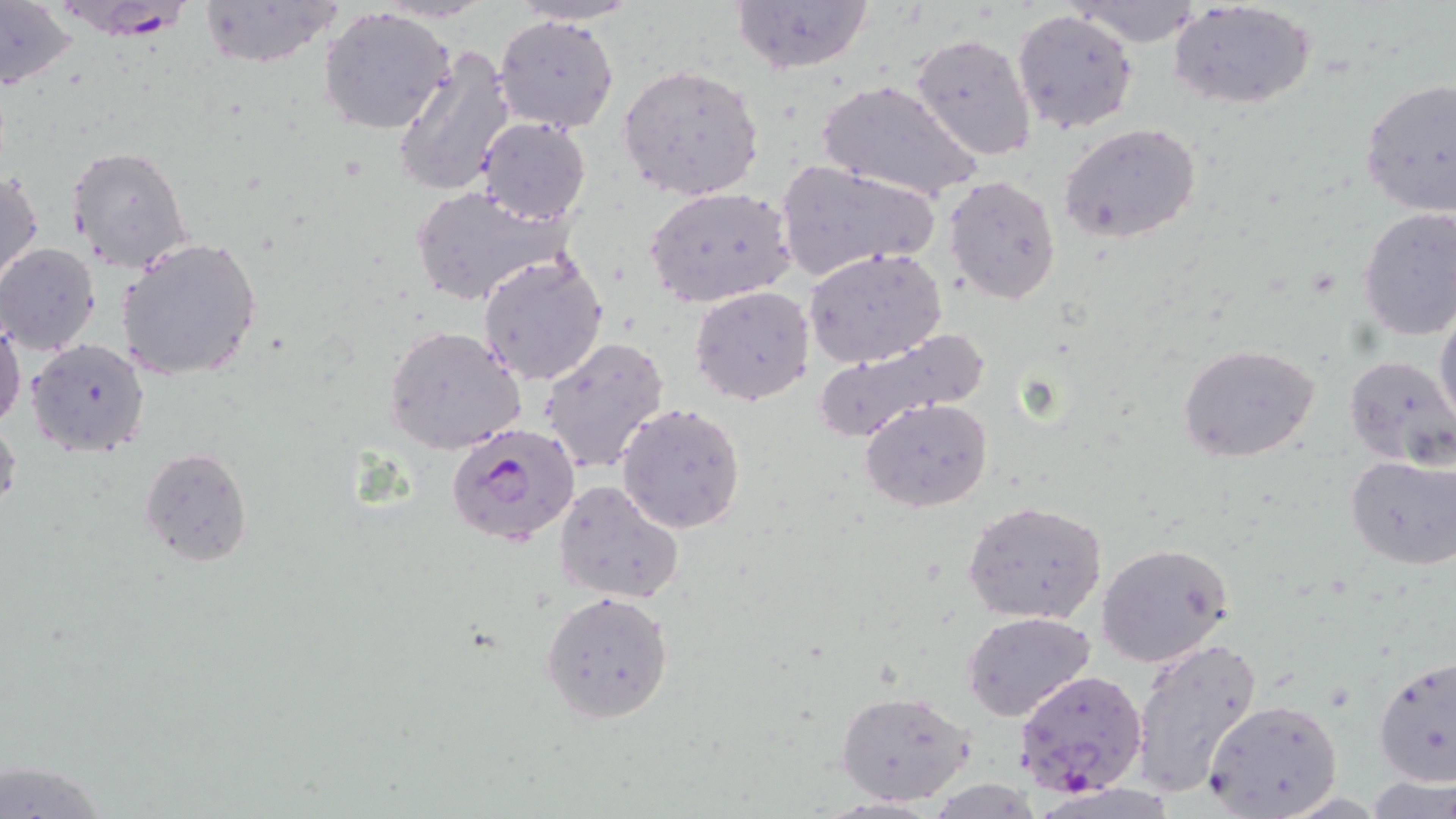
Plasmodium falciparum-infected red blood cell locations = approximate bounding boxes as (x1,y1)-(x2,y2) corner pairs in pixels: (47,0)-(202,40), (449,422)-(583,550), (1013,669)-(1146,796)
slide-level diagnosis = Plasmodium falciparum
field of view = single
stain = May-Grünwald-Giemsa
uninfected red blood cell locations = approximate bounding boxes as (x1,y1)-(x2,y2) corner pairs in pixels: (195,0)-(344,70), (729,0)-(874,75), (1070,0)-(1207,47), (0,1)-(81,92), (502,1)-(649,26), (1170,2)-(1317,112), (319,6)-(455,135), (1012,9)-(1139,135), (494,14)-(619,133), (910,32)-(1036,160), (391,43)-(518,200), (618,63)-(765,201), (1359,77)-(1456,218), (819,80)-(981,205), (475,117)-(591,225), (1058,123)-(1203,246), (66,144)-(192,271), (774,158)-(941,282), (1,168)-(43,292), (944,174)-(1063,305), (409,184)-(566,306), (645,186)-(796,311), (1357,208)-(1456,340), (115,237)-(264,382), (0,243)-(101,356), (805,247)-(949,367), (477,251)-(609,387), (690,286)-(815,404), (1434,298)-(1456,433), (0,309)-(24,433), (384,325)-(528,454), (811,329)-(991,440), (538,338)-(672,475), (25,339)-(152,458), (1179,344)-(1320,464), (1343,355)-(1456,467), (859,396)-(993,513), (617,404)-(747,534), (0,410)-(21,521), (139,447)-(254,566), (1344,453)-(1456,571), (555,479)-(687,604), (961,500)-(1109,626), (1096,542)-(1236,669), (541,591)-(675,723), (962,612)-(1096,722), (1129,635)-(1263,798), (1374,652)-(1455,787), (835,688)-(977,807), (1202,699)-(1343,819), (1,757)-(113,819)
magnification = 1000x
modality = optical microscopy
image size = 1456×819 pixels
preparation = thin blood film